Assess this cell for malaria.
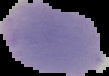

Uninfected.

preparation: thin blood smear
image_size: 109×76 pixels
image_type: segmented cell region with the area outside set to black